Outline each blood parasite and name the species.
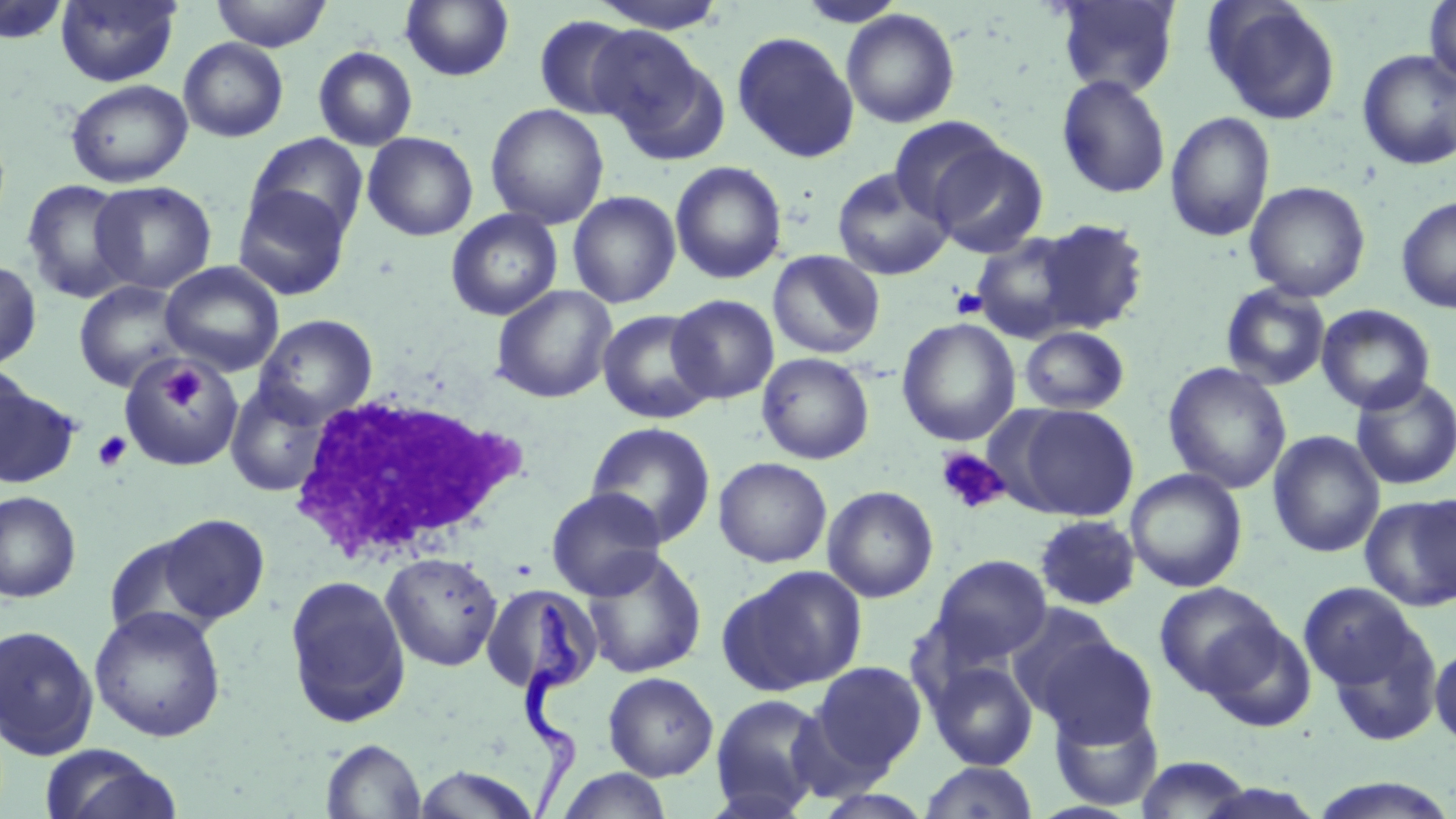

Approximate bounding boxes as [x1, y1, x2, y2] in pixels.
Trypanosoma brucei: [515, 599, 598, 815].
No Plasmodium falciparum, Plasmodium ovale, Plasmodium malariae, Plasmodium vivax, or Babesia divergens observed.

{
  "slide_level_diagnosis": "Trypanosoma brucei",
  "magnification": "1000x",
  "field_of_view": "one of a larger specimen",
  "platelet_locations": "approximate bounding boxes as [x1, y1, x2, y2] in pixels: [950, 287, 988, 319], [161, 366, 204, 410], [92, 431, 132, 472], [936, 447, 1010, 515]",
  "stain": "May-Grünwald-Giemsa",
  "modality": "light microscopy",
  "image_size": "1456×819 pixels",
  "preparation": "thin blood film",
  "uninfected_red_blood_cell_locations": "approximate bounding boxes as [x1, y1, x2, y2] in pixels: [210, 0, 332, 51], [588, 0, 729, 32], [797, 0, 907, 27], [1054, 0, 1181, 97], [1204, 0, 1343, 125], [1424, 0, 1456, 90], [0, 1, 73, 45], [55, 1, 181, 87], [400, 1, 514, 81], [841, 9, 960, 128], [533, 15, 642, 120], [588, 27, 719, 153], [732, 31, 859, 163], [178, 37, 288, 142], [313, 46, 418, 150], [1357, 49, 1456, 170], [1056, 74, 1171, 199], [65, 79, 193, 188], [485, 103, 609, 229], [1165, 110, 1275, 243], [887, 116, 1009, 223], [362, 131, 478, 241], [246, 133, 369, 243], [927, 140, 1048, 257], [670, 160, 788, 284], [831, 166, 954, 280], [569, 178, 787, 298], [21, 179, 138, 303], [89, 180, 217, 294], [1244, 181, 1371, 302], [232, 185, 353, 301], [567, 191, 681, 309], [1396, 195, 1456, 314], [445, 208, 563, 322], [1033, 219, 1149, 334], [970, 232, 1088, 344], [767, 250, 885, 359], [0, 260, 42, 371], [159, 261, 284, 377], [73, 280, 191, 392], [1221, 283, 1331, 391], [491, 285, 617, 404], [667, 294, 779, 404], [1317, 304, 1436, 414], [597, 309, 717, 424], [253, 313, 378, 426], [897, 318, 1021, 446], [1019, 325, 1130, 415], [756, 352, 875, 465], [117, 354, 245, 470], [1163, 362, 1292, 494], [0, 363, 36, 478], [1350, 375, 1456, 490], [1, 382, 81, 491], [225, 383, 333, 497], [1008, 403, 1139, 522], [585, 421, 717, 548], [1267, 430, 1384, 558], [713, 456, 832, 568], [1125, 468, 1248, 593], [822, 485, 939, 603], [545, 487, 668, 600], [0, 491, 81, 602], [1411, 492, 1455, 606], [1359, 494, 1456, 612], [155, 514, 270, 626], [1034, 514, 1141, 611], [104, 532, 220, 643], [581, 548, 708, 678], [381, 552, 504, 671], [929, 554, 1052, 668], [717, 565, 868, 696], [284, 574, 412, 728], [1298, 581, 1419, 693], [479, 582, 603, 696], [1154, 582, 1282, 697], [1005, 604, 1124, 715], [89, 606, 227, 742], [1323, 616, 1443, 747], [1202, 619, 1316, 733], [0, 624, 99, 759], [1036, 634, 1157, 747], [1430, 643, 1456, 749], [926, 659, 1039, 771], [809, 661, 927, 777], [603, 672, 719, 781], [709, 693, 832, 816], [1048, 704, 1164, 811], [321, 739, 425, 819], [38, 744, 183, 819], [1134, 756, 1254, 817], [920, 762, 1039, 818], [411, 765, 542, 818], [554, 767, 673, 819], [1305, 777, 1456, 818], [810, 789, 938, 819]",
  "white_blood_cell_locations": "approximate bounding boxes as [x1, y1, x2, y2] in pixels: [290, 390, 532, 564]"
}